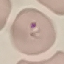

Summary:
  - Result: malaria parasites detected
  - Preparation: thin smear
  - Image type: cell patch, automatically extracted from a larger field of view and resized to 64 × 64 pixels
  - Stain: Giemsa
  - Capture: smartphone through the microscope eyepiece